Outline each Plasmodium falciparum-infected red blood cell.
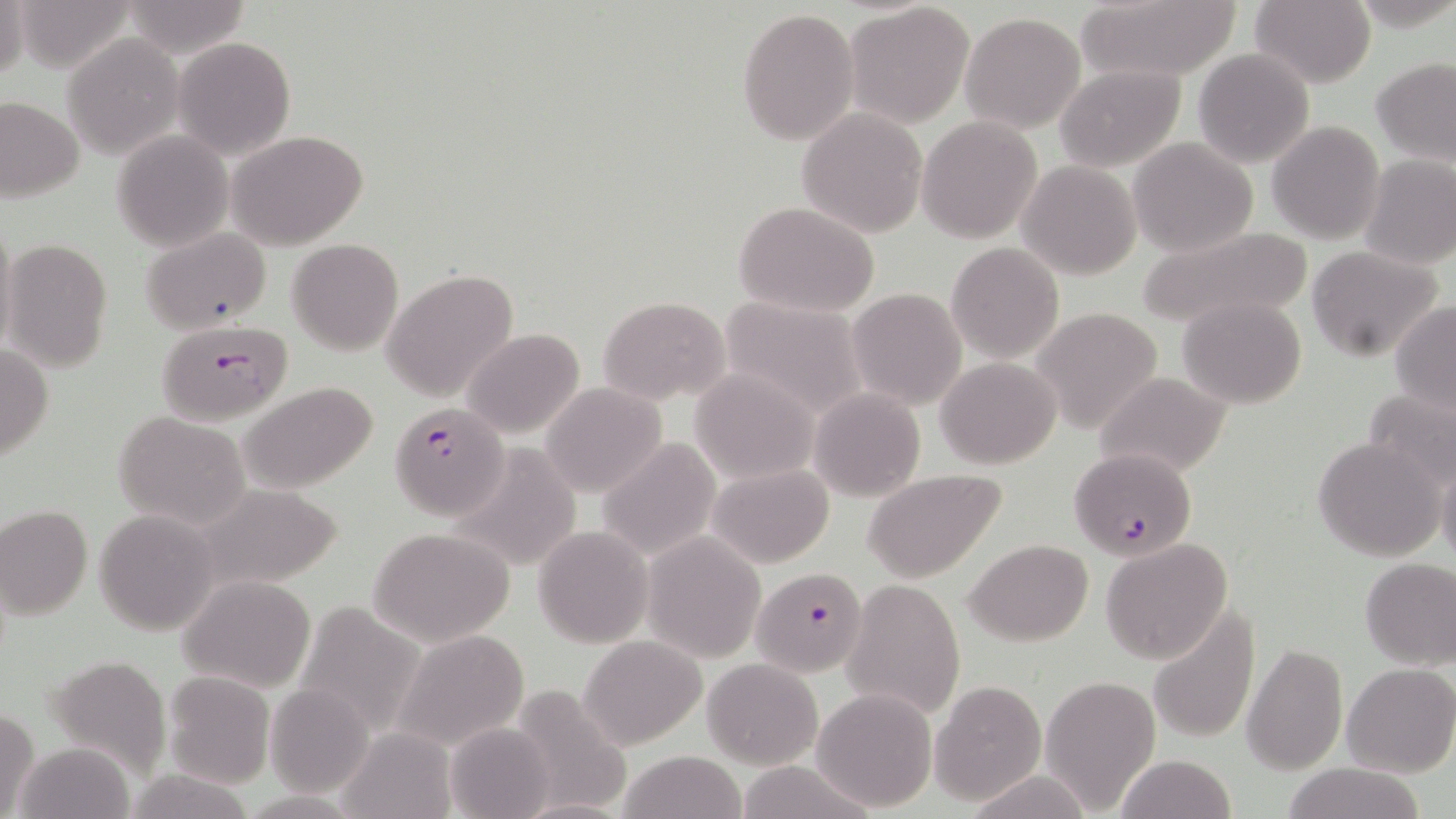
Approximate bounding boxes as named x1/y1/x2/y2 corners in pixels.
Plasmodium falciparum-infected red blood cells: (x1=157, y1=320, x2=291, y2=426), (x1=386, y1=397, x2=506, y2=515), (x1=1068, y1=448, x2=1196, y2=560), (x1=753, y1=568, x2=866, y2=675).

Summary:
  - Uninfected red blood cell locations: (x1=0, y1=0, x2=27, y2=85), (x1=1072, y1=0, x2=1245, y2=84), (x1=1251, y1=0, x2=1376, y2=88), (x1=121, y1=2, x2=253, y2=60), (x1=845, y1=3, x2=976, y2=128), (x1=736, y1=6, x2=858, y2=147), (x1=960, y1=12, x2=1086, y2=134), (x1=62, y1=32, x2=183, y2=160), (x1=173, y1=37, x2=296, y2=160), (x1=1192, y1=47, x2=1314, y2=169), (x1=1372, y1=60, x2=1455, y2=165), (x1=1055, y1=65, x2=1185, y2=171), (x1=0, y1=97, x2=84, y2=202), (x1=796, y1=109, x2=927, y2=237), (x1=917, y1=115, x2=1042, y2=244), (x1=1266, y1=120, x2=1384, y2=245), (x1=112, y1=130, x2=235, y2=251), (x1=226, y1=130, x2=369, y2=249), (x1=1127, y1=138, x2=1258, y2=257), (x1=1360, y1=153, x2=1456, y2=271), (x1=1019, y1=161, x2=1141, y2=278), (x1=734, y1=201, x2=881, y2=318), (x1=0, y1=217, x2=18, y2=362), (x1=1136, y1=224, x2=1311, y2=334), (x1=143, y1=228, x2=272, y2=333), (x1=3, y1=239, x2=113, y2=372), (x1=286, y1=239, x2=404, y2=355), (x1=946, y1=242, x2=1064, y2=362), (x1=1307, y1=246, x2=1445, y2=363), (x1=381, y1=269, x2=519, y2=402), (x1=847, y1=289, x2=967, y2=409), (x1=598, y1=295, x2=731, y2=407), (x1=718, y1=296, x2=869, y2=418), (x1=1178, y1=297, x2=1307, y2=407), (x1=1391, y1=302, x2=1456, y2=419), (x1=1031, y1=308, x2=1164, y2=432), (x1=460, y1=328, x2=584, y2=441), (x1=0, y1=344, x2=53, y2=462), (x1=937, y1=356, x2=1062, y2=468), (x1=690, y1=369, x2=818, y2=483), (x1=1093, y1=370, x2=1232, y2=479), (x1=242, y1=382, x2=378, y2=495), (x1=541, y1=382, x2=667, y2=498), (x1=1361, y1=386, x2=1456, y2=495), (x1=809, y1=388, x2=926, y2=502), (x1=115, y1=411, x2=250, y2=528), (x1=1314, y1=435, x2=1444, y2=561), (x1=596, y1=437, x2=724, y2=560), (x1=446, y1=444, x2=583, y2=572), (x1=1436, y1=458, x2=1456, y2=564), (x1=708, y1=464, x2=835, y2=567), (x1=863, y1=468, x2=1008, y2=581), (x1=0, y1=504, x2=93, y2=619), (x1=93, y1=508, x2=221, y2=635), (x1=534, y1=526, x2=652, y2=647), (x1=370, y1=527, x2=516, y2=645), (x1=642, y1=533, x2=766, y2=662), (x1=1101, y1=538, x2=1233, y2=664), (x1=964, y1=539, x2=1094, y2=646), (x1=1358, y1=557, x2=1456, y2=670), (x1=179, y1=577, x2=315, y2=693), (x1=841, y1=579, x2=967, y2=719), (x1=290, y1=601, x2=430, y2=741), (x1=1148, y1=607, x2=1259, y2=744), (x1=393, y1=628, x2=531, y2=752), (x1=578, y1=636, x2=707, y2=750), (x1=1242, y1=642, x2=1348, y2=774), (x1=42, y1=653, x2=173, y2=778), (x1=702, y1=657, x2=822, y2=770), (x1=1343, y1=663, x2=1456, y2=778), (x1=162, y1=672, x2=274, y2=789), (x1=1040, y1=675, x2=1160, y2=812), (x1=929, y1=679, x2=1047, y2=805), (x1=266, y1=684, x2=373, y2=797), (x1=509, y1=685, x2=631, y2=818), (x1=811, y1=687, x2=937, y2=811), (x1=1, y1=706, x2=41, y2=818), (x1=445, y1=723, x2=555, y2=818), (x1=337, y1=728, x2=458, y2=818), (x1=14, y1=741, x2=136, y2=818), (x1=616, y1=750, x2=743, y2=819), (x1=1113, y1=754, x2=1239, y2=819), (x1=733, y1=761, x2=878, y2=819), (x1=1279, y1=762, x2=1431, y2=819), (x1=966, y1=772, x2=1093, y2=818), (x1=516, y1=798, x2=634, y2=819)
  - Slide-level diagnosis: Plasmodium falciparum
  - Modality: optical microscopy
  - Field of view: one of a larger specimen
  - Preparation: thin blood film
  - Image size: 1456×819 pixels
  - Stain: May-Grünwald-Giemsa
  - Magnification: 1000x